Evaluate for malaria.
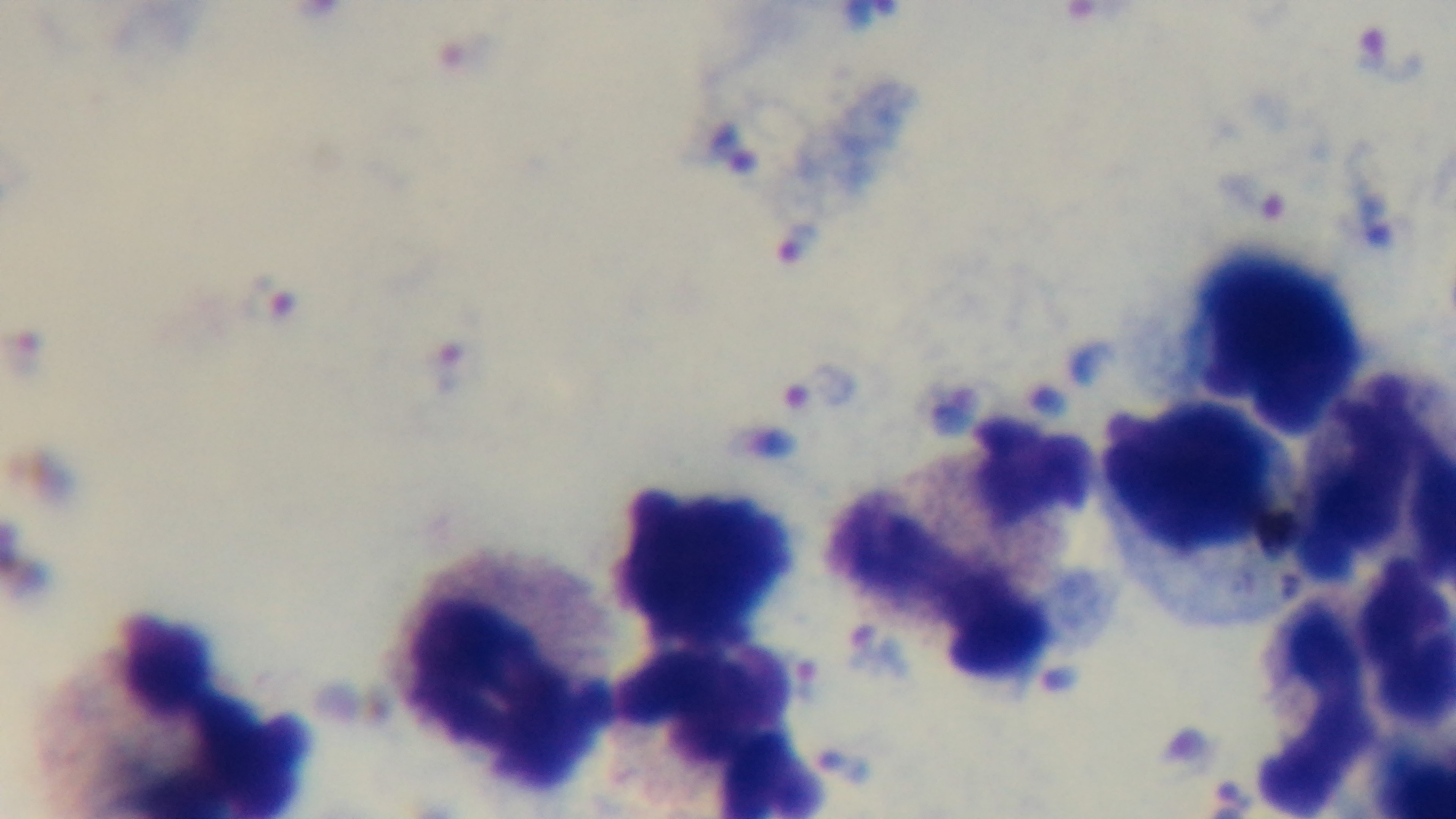

Infected.

Summary:
  - Stain: Giemsa
  - Modality: light microscopy
  - Capture: mounted 4K digital camera
  - Preparation: thick blood film
  - Objective: 100x oil immersion
  - Field of view: one from the slide